Name the parasite shown.
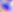
Toxoplasma gondii.

Summary:
  - Modality: micrograph
  - Magnification: 400x